Describe the morphology of the erythrocytes.
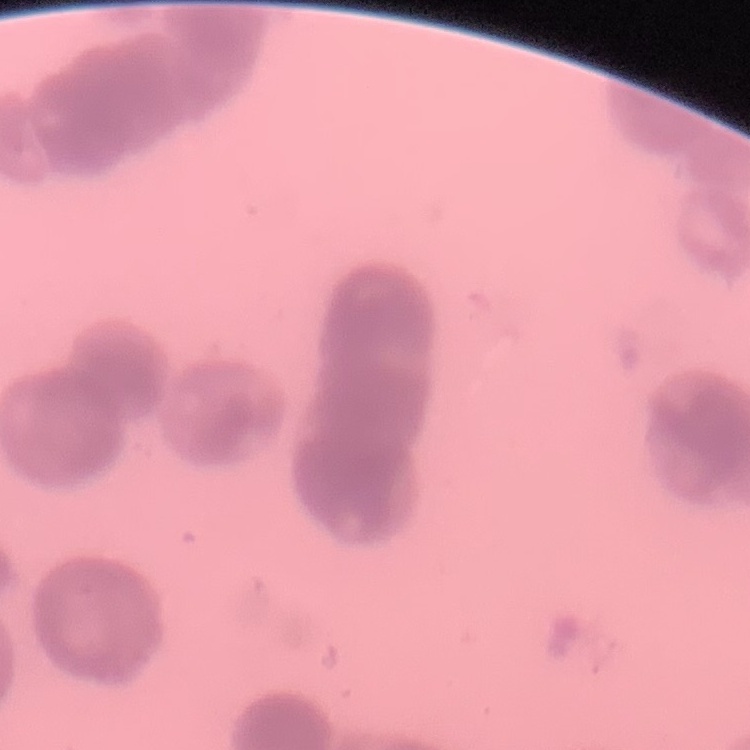
They show rouleaux formation.

Field's or Giemsa stain. Square crop of a larger photomicrograph. Thin peripheral smear.